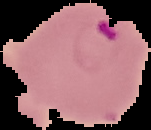
{
  "malaria_status": "parasitized",
  "image_size": "151×130 pixels",
  "image_type": "segmented cell region on a black background",
  "preparation": "thin blood film"
}